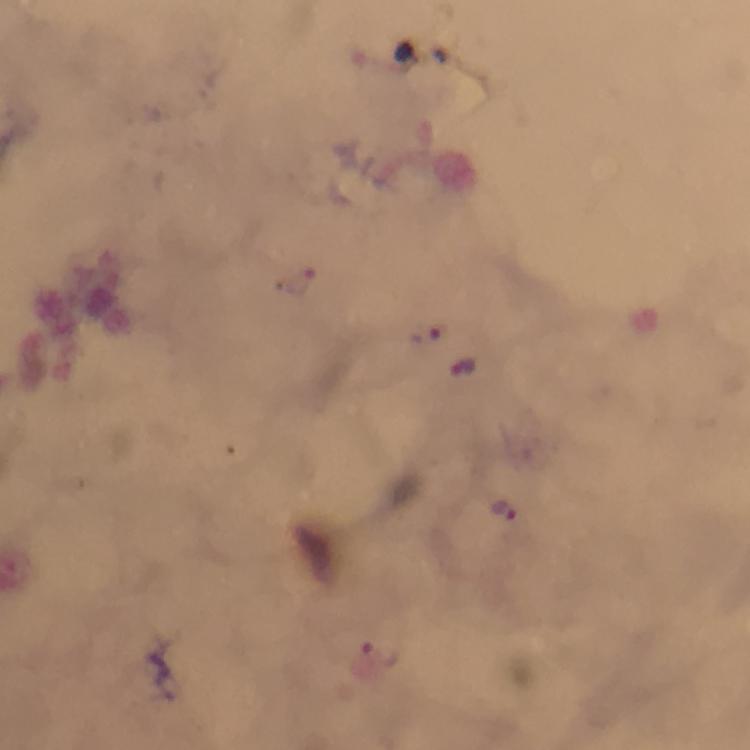

magnification = 100x
stain = Giemsa
image size = 750×750 pixels
capture = smartphone camera through the microscope
context = from a malaria diagnostic workup
immersion oil = used
Plasmodium parasite locations = approximate centers as [x, y] in pixels: [300, 280], [425, 333], [464, 367], [501, 509], [379, 656]
cropped from = one field of view
preparation = thick blood smear